Classify this cell by malaria status.
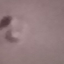

It is parasitized.

capture = smartphone camera at the microscope eyepiece
preparation = thin smear
image type = automatically extracted cell patch, resized to 64 × 64 pixels
stain = Giemsa